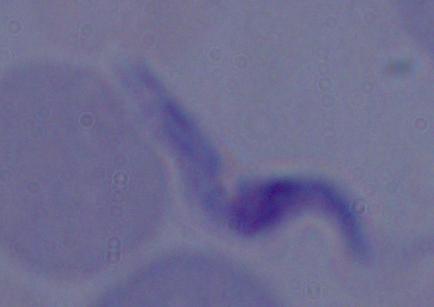

Summary:
  - Magnification: 1000x
  - Modality: micrograph
  - Identification: trypanosome